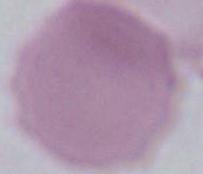

Summary:
  - Identification: red blood cell
  - Modality: photomicrograph
  - Magnification: 1000x